Classify this cell by malaria status.
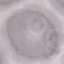

Uninfected.

Summary:
  - Preparation: thin blood smear
  - Image type: cell patch, automatically extracted from a larger field of view and resized to 64 × 64 pixels
  - Capture: smartphone camera at the microscope eyepiece
  - Stain: Giemsa